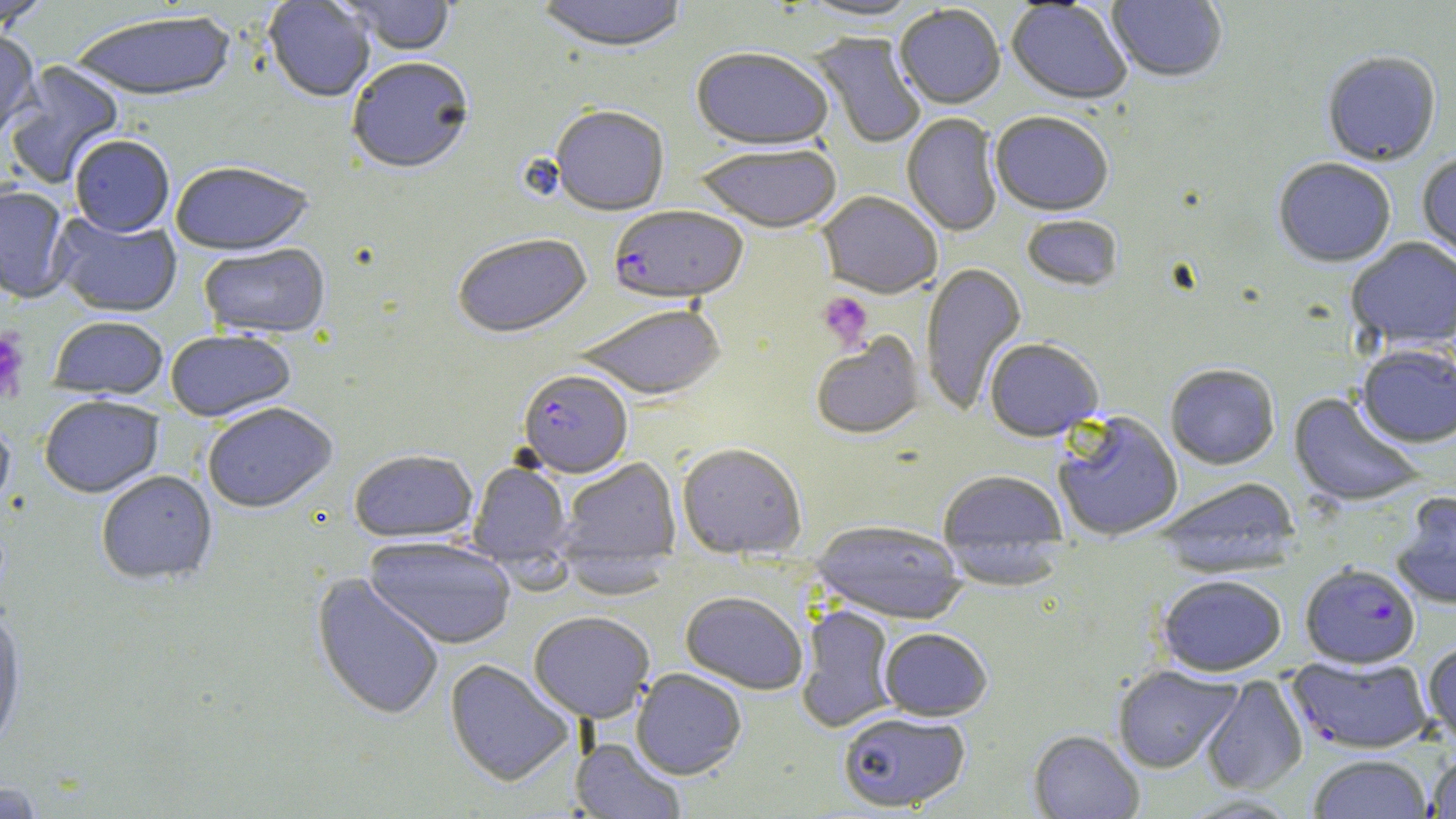
Summary:
  - Coordinate format: approximate bounding boxes as named x1/y1/x2/y2 corners in pixels
  - Plasmodium falciparum-infected red blood cell locations: (x1=609, y1=206, x2=748, y2=304), (x1=518, y1=370, x2=632, y2=478), (x1=1300, y1=563, x2=1420, y2=669), (x1=1288, y1=655, x2=1432, y2=754)
  - Uninfected red blood cell locations: (x1=0, y1=0, x2=54, y2=33), (x1=263, y1=0, x2=375, y2=104), (x1=338, y1=0, x2=457, y2=56), (x1=534, y1=0, x2=690, y2=54), (x1=794, y1=0, x2=926, y2=23), (x1=1106, y1=0, x2=1227, y2=85), (x1=1006, y1=1, x2=1131, y2=105), (x1=894, y1=5, x2=1006, y2=109), (x1=71, y1=12, x2=236, y2=104), (x1=0, y1=30, x2=40, y2=144), (x1=810, y1=32, x2=927, y2=149), (x1=691, y1=47, x2=834, y2=150), (x1=1321, y1=54, x2=1441, y2=168), (x1=347, y1=58, x2=474, y2=176), (x1=3, y1=61, x2=124, y2=190), (x1=550, y1=105, x2=670, y2=217), (x1=990, y1=112, x2=1114, y2=217), (x1=901, y1=114, x2=1002, y2=237), (x1=69, y1=136, x2=174, y2=238), (x1=694, y1=142, x2=843, y2=233), (x1=1416, y1=153, x2=1456, y2=268), (x1=1273, y1=159, x2=1396, y2=268), (x1=170, y1=163, x2=314, y2=257), (x1=0, y1=185, x2=73, y2=304), (x1=817, y1=191, x2=943, y2=299), (x1=51, y1=212, x2=182, y2=318), (x1=1021, y1=215, x2=1124, y2=292), (x1=453, y1=233, x2=593, y2=338), (x1=1346, y1=238, x2=1456, y2=351), (x1=198, y1=244, x2=331, y2=340), (x1=920, y1=262, x2=1026, y2=415), (x1=574, y1=303, x2=726, y2=400), (x1=49, y1=317, x2=168, y2=399), (x1=165, y1=329, x2=296, y2=421), (x1=810, y1=332, x2=925, y2=440), (x1=984, y1=338, x2=1104, y2=441), (x1=1356, y1=345, x2=1456, y2=448), (x1=1165, y1=363, x2=1280, y2=470), (x1=1289, y1=392, x2=1425, y2=509), (x1=40, y1=396, x2=163, y2=498), (x1=202, y1=402, x2=337, y2=514), (x1=1053, y1=411, x2=1184, y2=541), (x1=0, y1=420, x2=15, y2=517), (x1=677, y1=442, x2=807, y2=559), (x1=349, y1=449, x2=478, y2=542), (x1=557, y1=457, x2=681, y2=567), (x1=469, y1=461, x2=573, y2=568), (x1=938, y1=470, x2=1069, y2=576), (x1=96, y1=471, x2=218, y2=586), (x1=1153, y1=477, x2=1301, y2=575), (x1=1391, y1=491, x2=1456, y2=609), (x1=810, y1=521, x2=967, y2=624), (x1=364, y1=536, x2=515, y2=650), (x1=310, y1=572, x2=446, y2=722), (x1=1156, y1=574, x2=1287, y2=676), (x1=680, y1=590, x2=808, y2=694), (x1=797, y1=605, x2=898, y2=733), (x1=528, y1=611, x2=655, y2=723), (x1=0, y1=612, x2=27, y2=755), (x1=879, y1=627, x2=992, y2=720), (x1=1423, y1=641, x2=1456, y2=750), (x1=444, y1=659, x2=575, y2=787), (x1=1112, y1=665, x2=1241, y2=773), (x1=631, y1=669, x2=747, y2=779), (x1=1201, y1=677, x2=1308, y2=796), (x1=837, y1=711, x2=971, y2=812), (x1=1028, y1=729, x2=1144, y2=819), (x1=570, y1=738, x2=687, y2=818), (x1=1426, y1=749, x2=1456, y2=817), (x1=1308, y1=754, x2=1432, y2=818), (x1=1, y1=780, x2=48, y2=817)
  - Platelet locations: (x1=818, y1=291, x2=874, y2=350), (x1=0, y1=329, x2=30, y2=403)
  - Slide-level diagnosis: Plasmodium falciparum
  - Preparation: thin blood film
  - Field of view: single
  - Magnification: 1000x
  - Modality: light microscopy
  - Stain: May-Grünwald-Giemsa
  - Image size: 1456×819 pixels